State which cell type is depicted.
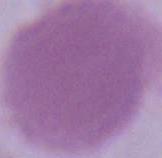

An erythrocyte.

modality: photomicrograph
magnification: 1000x